Classify this cell by malaria status.
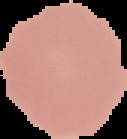
It is uninfected.

image_size: 127×139 pixels
image_type: cell region segmented out of the field of view; surrounding area masked to black
preparation: thin blood smear